Classify this cell by malaria status.
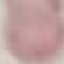
It is uninfected.

image_type: cell patch, automatically extracted from a larger field of view and resized to 64 × 64 pixels
stain: Giemsa
capture: smartphone through the microscope eyepiece
preparation: thin blood film